Locate and identify every blood parasite.
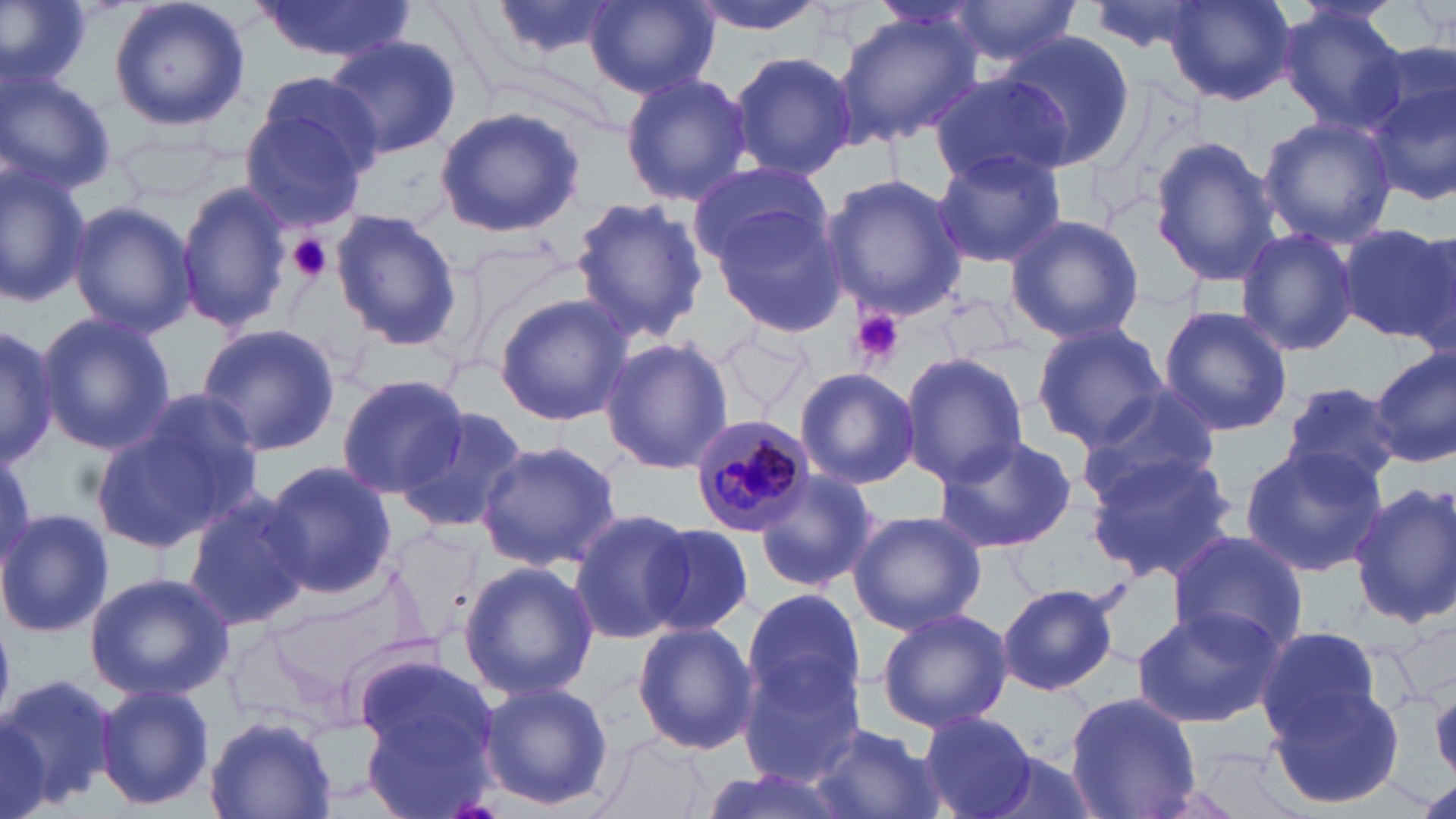
Approximate bounding boxes as (x1, y1, x2, y2) in pixels.
Plasmodium malariae-infected red blood cells: (687, 412, 818, 537).
No Plasmodium falciparum, Plasmodium ovale, Plasmodium vivax, Babesia divergens, or Trypanosoma brucei observed.

Uninfected red blood cell locations: (0, 0, 92, 92), (106, 0, 251, 133), (487, 0, 624, 63), (684, 0, 830, 35), (938, 0, 1084, 68), (1084, 0, 1213, 57), (250, 1, 413, 62), (584, 1, 717, 98), (1164, 1, 1294, 106), (1276, 4, 1407, 134), (836, 11, 982, 144), (995, 31, 1136, 170), (324, 34, 460, 161), (728, 50, 855, 181), (0, 65, 117, 197), (620, 70, 751, 205), (1363, 71, 1456, 208), (930, 76, 1068, 186), (244, 80, 378, 229), (434, 105, 586, 239), (1257, 115, 1398, 247), (1150, 136, 1281, 288), (933, 148, 1065, 269), (686, 159, 833, 267), (0, 161, 90, 308), (821, 173, 966, 321), (176, 181, 294, 332), (568, 195, 708, 344), (67, 199, 197, 338), (709, 204, 847, 339), (330, 208, 462, 349), (1004, 213, 1145, 346), (1337, 222, 1455, 343), (1236, 226, 1361, 356), (492, 293, 633, 428), (1158, 305, 1294, 435), (34, 310, 174, 456), (194, 323, 340, 458), (1031, 324, 1169, 450), (0, 326, 61, 466), (710, 329, 819, 415), (598, 337, 735, 473), (1370, 348, 1455, 465), (900, 350, 1028, 487), (793, 367, 921, 490), (337, 374, 469, 498), (1281, 381, 1402, 491), (1077, 394, 1220, 503), (95, 400, 259, 555), (394, 407, 528, 533), (932, 433, 1077, 556), (474, 440, 623, 572), (1239, 445, 1389, 576), (1086, 450, 1244, 586), (261, 460, 397, 599), (751, 468, 882, 594), (1350, 481, 1456, 629), (183, 490, 313, 633), (0, 508, 113, 641), (569, 509, 698, 647), (846, 510, 987, 635), (387, 522, 488, 646), (640, 523, 755, 640), (1166, 530, 1311, 659), (459, 559, 597, 700), (84, 570, 232, 702), (996, 581, 1122, 696), (741, 586, 867, 714), (873, 607, 1013, 732), (1132, 607, 1283, 728), (632, 622, 758, 756), (1254, 623, 1386, 744), (354, 652, 499, 775), (736, 653, 869, 786), (1, 674, 119, 816), (477, 680, 614, 811), (1270, 682, 1407, 813), (95, 683, 215, 811), (1063, 693, 1202, 819), (362, 707, 499, 819), (917, 709, 1036, 819), (206, 711, 336, 817), (807, 724, 946, 819), (588, 736, 714, 819), (971, 746, 1104, 819), (699, 767, 851, 818). Platelet locations: (288, 233, 334, 284), (850, 308, 906, 367). Slide-level diagnosis: Plasmodium malariae. May-Grünwald-Giemsa-stained preparation. 1000x magnification. Optical microscopy. Thin blood film. Image is 1456×819 pixels. Single field of view.